Draw a bounding box around every leukocyte (white blood cell).
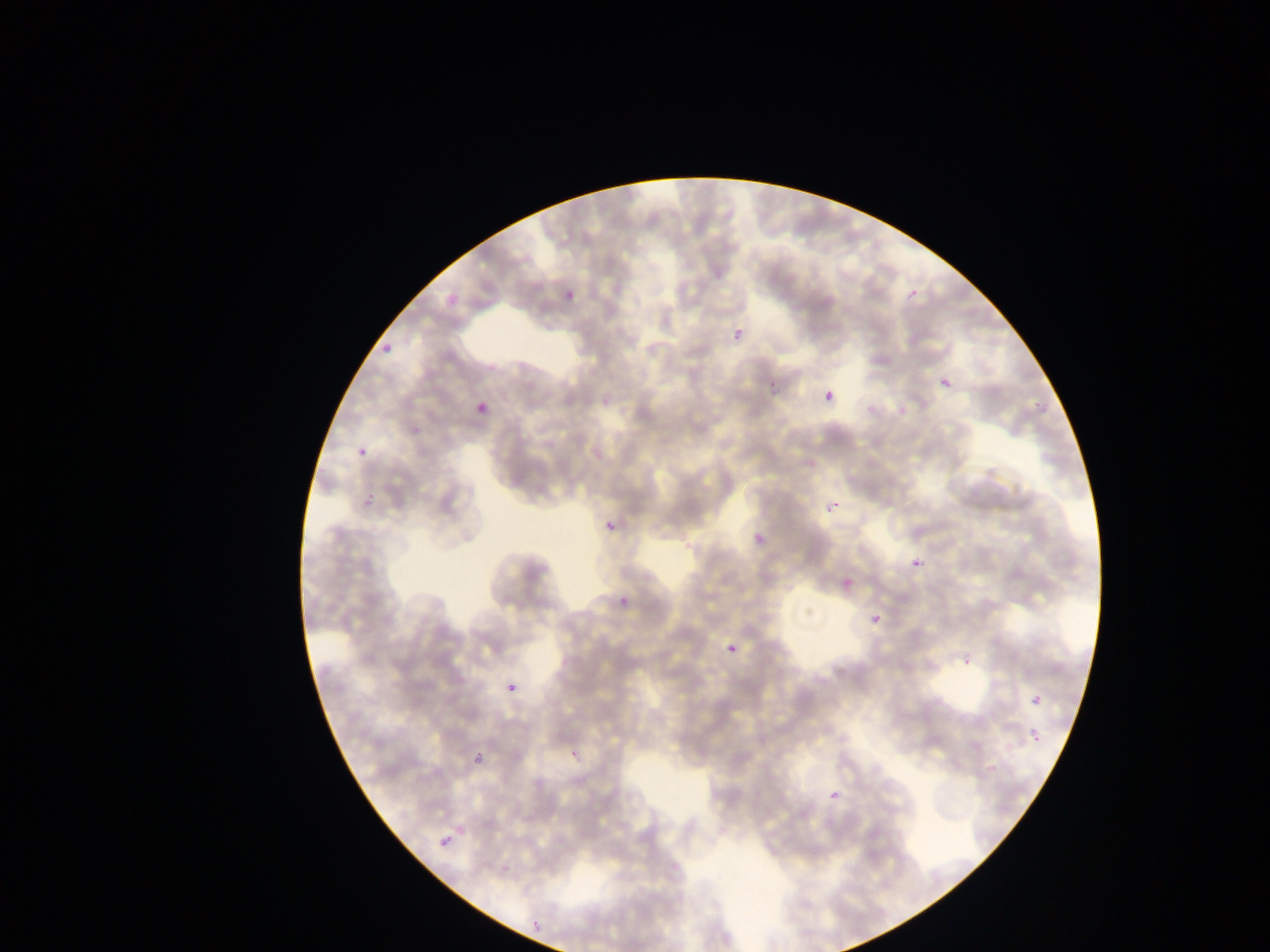

No leukocytes observed.

field_of_view: single
image_size: 1270×952 pixels
capture: mobile-phone photograph through a microscope
malaria_parasite_locations: 'approximate bounding boxes as [left, top, right, bottom] in pixels: [560, 285, 582, 311], [906, 286, 922, 304], [443, 287, 459, 305], [732, 328, 747, 345], [378, 339, 401, 352], [938, 375, 956, 395], [823, 390, 837, 406], [474, 400, 491, 420], [355, 444, 372, 462], [363, 491, 380, 508], [822, 493, 849, 523], [601, 506, 625, 536], [745, 531, 767, 548], [907, 552, 927, 575], [835, 570, 863, 601], [613, 592, 635, 615], [866, 608, 889, 632], [723, 639, 744, 662], [959, 654, 970, 672], [507, 683, 518, 695], [1026, 689, 1049, 714], [1026, 726, 1047, 749], [564, 743, 587, 769], [474, 756, 485, 771], [826, 788, 844, 807], [438, 834, 453, 852], [531, 919, 544, 931]'
preparation: thin blood film
country: Ghana